State which parasite is depicted.
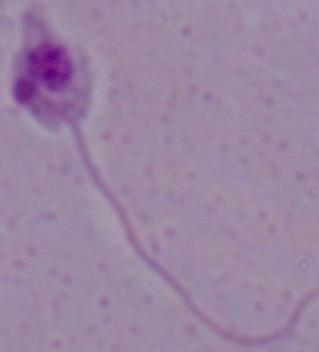
Leishmania.

{
  "modality": "photomicrograph",
  "magnification": "1000x"
}